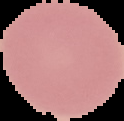 From a thin blood film. Malaria status: uninfected. Image is 124×121 pixels. The area outside the segmented cell region is set to black.